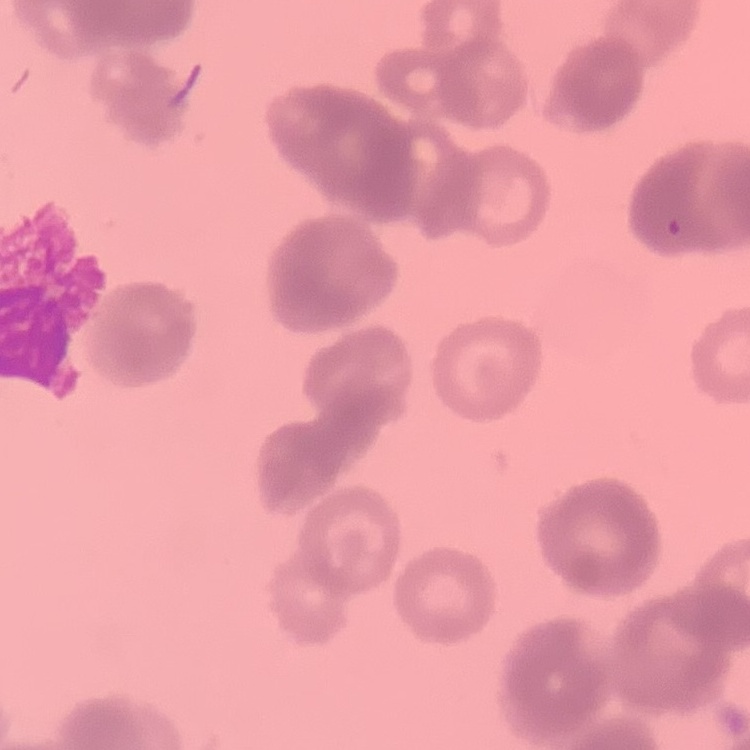

erythrocyte morphology = rouleaux formation
image type = square crop of a larger photomicrograph
preparation = thin blood film
stain = Field's or Giemsa